State the blood parasite species.
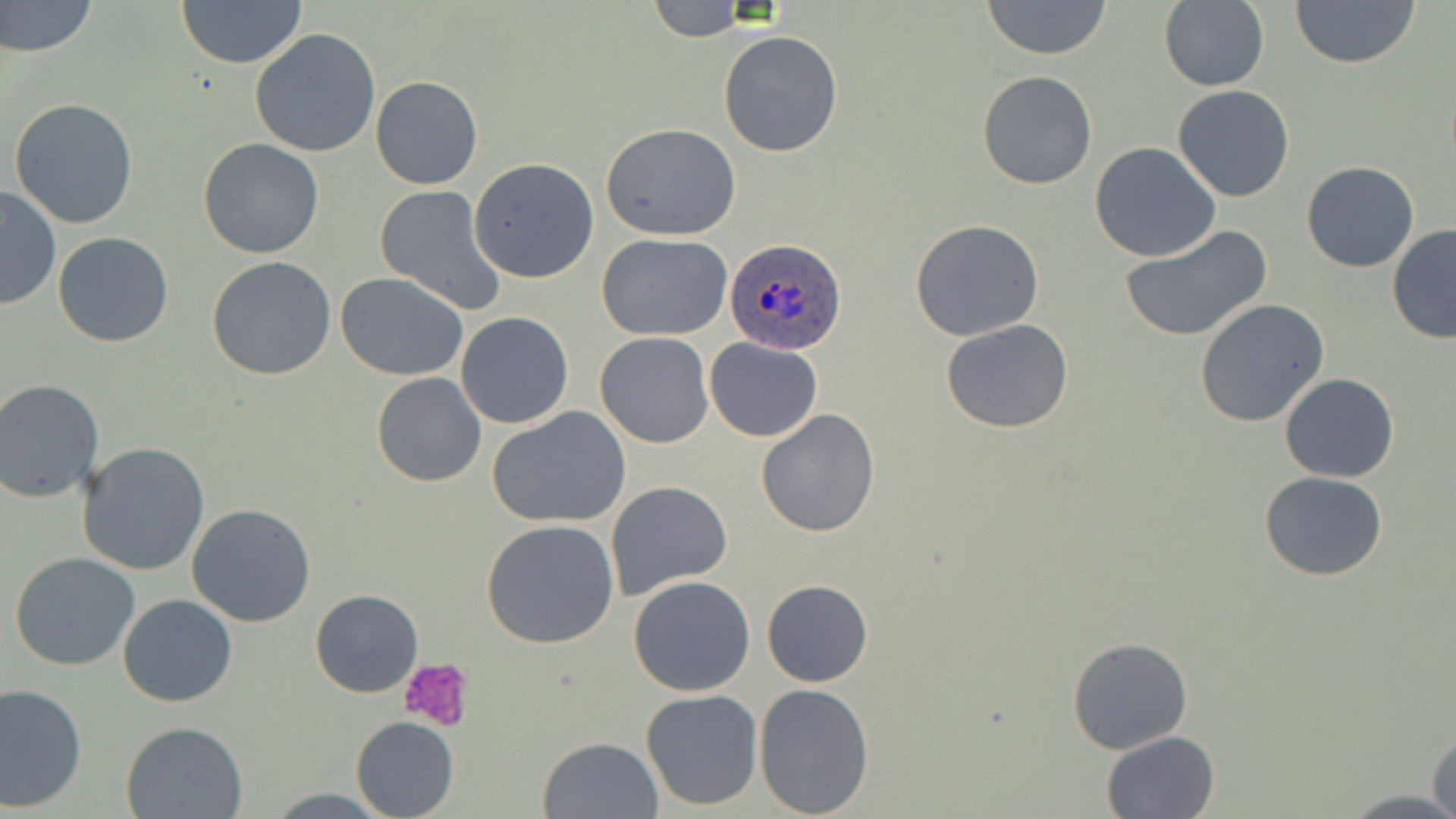

Plasmodium ovale.

preparation = thin blood film
platelet locations = approximate bounding boxes as [x1, y1, x2, y2] in pixels: [400, 656, 475, 731]
field of view = one of a larger specimen
stain = May-Grünwald-Giemsa
Plasmodium ovale-infected red blood cell locations = approximate bounding boxes as [x1, y1, x2, y2] in pixels: [724, 237, 845, 356]
uninfected red blood cell locations = approximate bounding boxes as [x1, y1, x2, y2] in pixels: [0, 0, 99, 58], [177, 0, 308, 69], [981, 0, 1112, 61], [1158, 0, 1270, 92], [1290, 0, 1420, 69], [644, 2, 755, 41], [249, 28, 381, 158], [717, 29, 844, 158], [976, 70, 1098, 191], [370, 76, 483, 190], [1172, 84, 1294, 203], [9, 97, 140, 229], [600, 124, 740, 240], [198, 139, 326, 258], [1090, 142, 1221, 263], [469, 158, 595, 281], [1302, 161, 1419, 273], [374, 184, 506, 315], [0, 186, 60, 311], [909, 218, 1044, 341], [1121, 225, 1273, 343], [1387, 225, 1456, 344], [53, 232, 175, 348], [596, 234, 734, 342], [207, 256, 336, 381], [336, 272, 470, 380], [1194, 298, 1330, 427], [456, 312, 574, 428], [940, 319, 1073, 434], [594, 331, 714, 449], [704, 338, 822, 442], [372, 373, 488, 488], [1280, 373, 1399, 482], [0, 382, 103, 503], [487, 406, 632, 528], [756, 409, 881, 537], [76, 443, 210, 576], [1260, 470, 1387, 581], [605, 481, 732, 602], [185, 503, 316, 628], [481, 519, 621, 650], [10, 552, 141, 671], [627, 574, 756, 697], [761, 578, 874, 687], [310, 589, 423, 696], [117, 594, 238, 707], [1066, 637, 1194, 755], [0, 684, 87, 810], [753, 684, 874, 816], [640, 690, 764, 810], [351, 716, 459, 818], [120, 720, 248, 818], [1428, 730, 1456, 818], [1100, 731, 1220, 819], [539, 736, 662, 818]
image size = 1456×819 pixels
magnification = 1000x
modality = light microscopy